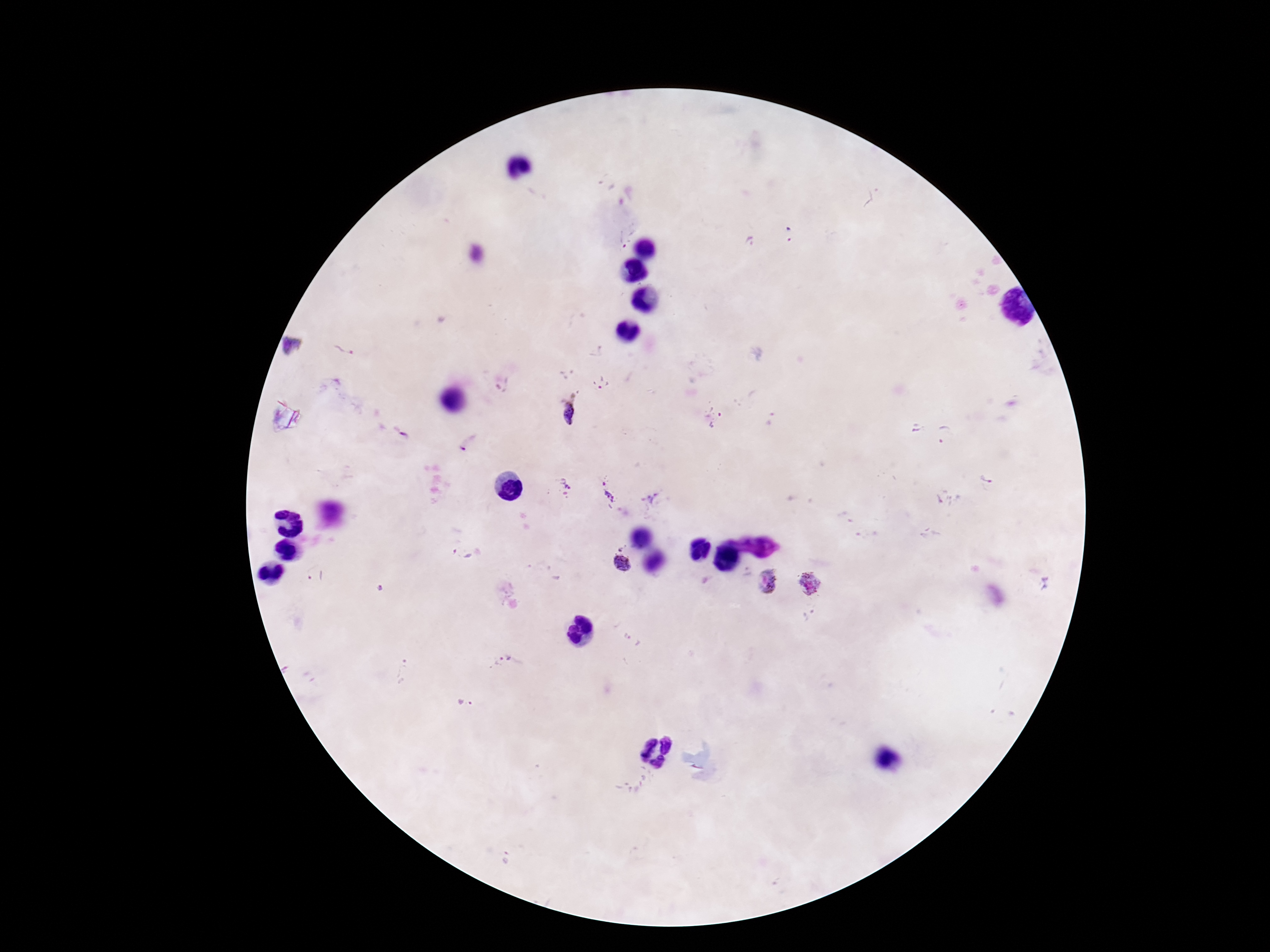
{
  "image_size": "1270×952 pixels",
  "patient_malaria_status": "infected",
  "magnification": "100x",
  "preparation": "thick peripheral-blood smear",
  "plasmodium_parasite_locations": "approximate centers as [x, y] in pixels: [789, 234], [621, 240], [749, 242], [294, 346], [347, 346], [596, 352], [567, 375], [602, 383], [505, 388], [568, 414], [714, 416], [917, 428], [400, 434], [945, 434], [468, 443], [987, 482], [563, 486], [608, 490], [649, 496], [461, 553], [621, 562], [316, 579], [767, 582], [809, 584], [506, 657], [404, 670], [466, 704]",
  "stain": "Giemsa",
  "capture": "smartphone camera through the microscope eyepiece",
  "field_of_view": "single"
}